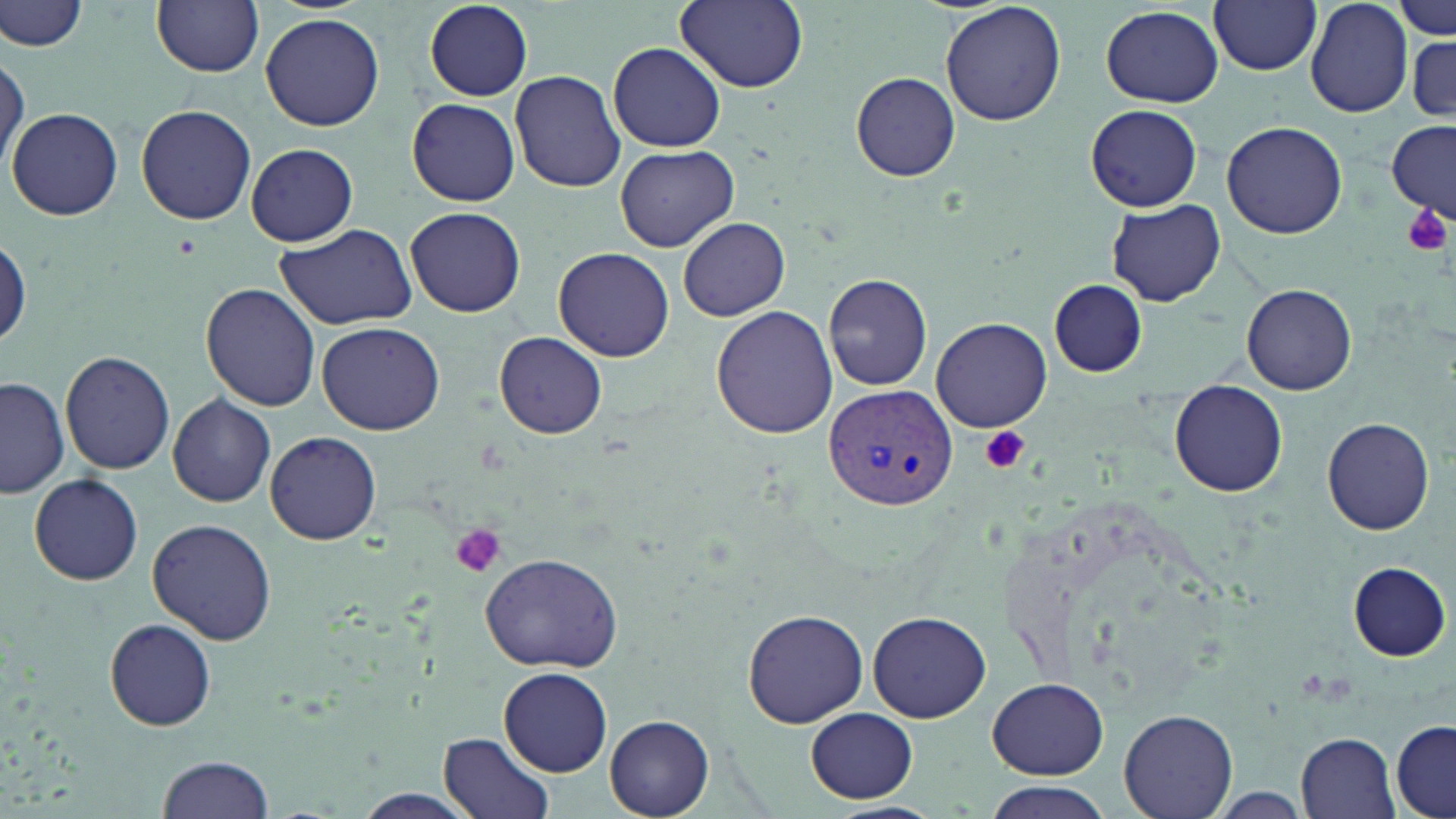 Approximate bounding boxes as [x1, y1, x2, y2] in pixels. Plasmodium vivax-infected red blood cell locations: [827, 384, 955, 510]. Platelet locations: [1403, 204, 1451, 257], [977, 426, 1031, 475], [451, 524, 506, 577]. Uninfected red blood cell locations: [422, 0, 535, 102], [674, 0, 809, 91], [940, 0, 1066, 128], [1209, 0, 1322, 75], [1396, 0, 1453, 42], [2, 1, 89, 52], [153, 1, 265, 77], [1306, 1, 1413, 117], [1100, 4, 1224, 109], [261, 13, 384, 131], [1402, 27, 1456, 120], [609, 42, 727, 151], [0, 51, 27, 172], [510, 69, 626, 193], [851, 71, 960, 181], [407, 99, 519, 205], [134, 103, 257, 225], [1086, 104, 1203, 210], [9, 106, 123, 220], [1222, 120, 1348, 239], [1387, 121, 1455, 219], [244, 143, 359, 246], [615, 143, 739, 252], [1106, 199, 1225, 307], [405, 207, 526, 317], [678, 217, 790, 320], [275, 222, 415, 328], [0, 233, 29, 351], [553, 246, 674, 362], [823, 272, 934, 391], [1049, 279, 1148, 377], [1242, 283, 1358, 393], [201, 284, 322, 411], [710, 305, 839, 439], [931, 317, 1053, 432], [316, 321, 444, 435], [493, 332, 607, 440], [60, 351, 176, 476], [0, 377, 70, 499], [1170, 380, 1286, 496], [167, 394, 276, 507], [1322, 417, 1434, 535], [264, 432, 381, 543], [28, 472, 144, 585], [147, 517, 277, 645], [477, 551, 627, 676], [1349, 562, 1450, 660], [742, 607, 868, 728], [868, 610, 991, 722], [103, 618, 217, 731], [499, 668, 613, 777], [989, 678, 1107, 778], [807, 709, 917, 802], [1117, 709, 1238, 819], [606, 715, 714, 818], [1390, 718, 1456, 819], [439, 730, 556, 819], [1296, 731, 1399, 819], [157, 754, 276, 819], [984, 785, 1110, 819], [344, 790, 488, 819], [822, 803, 944, 819]. Slide-level diagnosis: Plasmodium vivax. May-Grünwald-Giemsa-stained preparation. Image is 1456×819 pixels. Thin blood film. 1000x magnification. Single field of view. Optical microscopy.